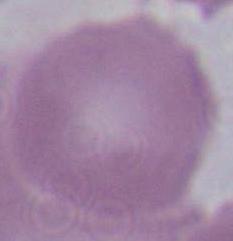
Summary:
  - Magnification: 1000x
  - Modality: micrograph
  - Identification: red blood cell